Name the parasite shown.
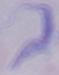

This is a trypanosome.

magnification = 1000x
modality = photomicrograph